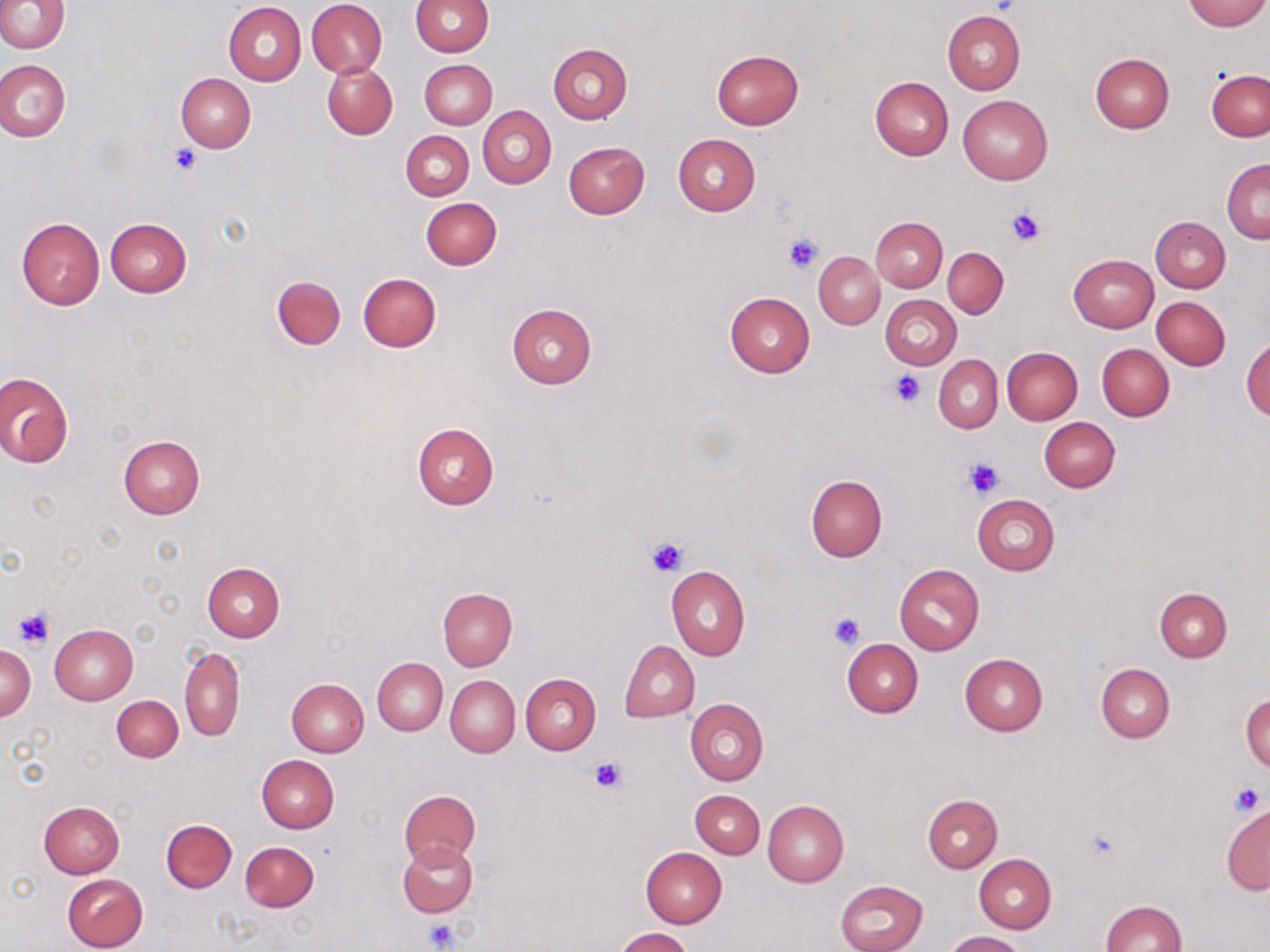 Approximate bounding boxes as named x1/y1/x2/y2 corners in pixels. Platelet locations: (x1=987, y1=0, x2=1021, y2=16), (x1=171, y1=145, x2=200, y2=174), (x1=1005, y1=206, x2=1047, y2=250), (x1=783, y1=232, x2=822, y2=273), (x1=887, y1=371, x2=924, y2=408), (x1=962, y1=457, x2=1007, y2=500), (x1=644, y1=536, x2=688, y2=577), (x1=13, y1=608, x2=55, y2=647), (x1=829, y1=612, x2=864, y2=649), (x1=590, y1=756, x2=625, y2=792), (x1=1230, y1=782, x2=1266, y2=814), (x1=424, y1=918, x2=458, y2=952). Uninfected red blood cell locations: (x1=0, y1=0, x2=68, y2=53), (x1=307, y1=0, x2=387, y2=78), (x1=413, y1=0, x2=493, y2=56), (x1=1183, y1=0, x2=1269, y2=30), (x1=223, y1=3, x2=306, y2=85), (x1=941, y1=12, x2=1024, y2=94), (x1=548, y1=44, x2=632, y2=124), (x1=711, y1=50, x2=803, y2=130), (x1=1089, y1=52, x2=1173, y2=132), (x1=0, y1=58, x2=70, y2=142), (x1=420, y1=59, x2=496, y2=128), (x1=322, y1=61, x2=398, y2=140), (x1=1206, y1=70, x2=1269, y2=141), (x1=176, y1=74, x2=255, y2=152), (x1=869, y1=76, x2=953, y2=160), (x1=958, y1=95, x2=1052, y2=185), (x1=478, y1=106, x2=556, y2=189), (x1=401, y1=130, x2=474, y2=201), (x1=673, y1=133, x2=760, y2=215), (x1=564, y1=142, x2=650, y2=218), (x1=1221, y1=159, x2=1270, y2=244), (x1=421, y1=198, x2=502, y2=269), (x1=1151, y1=216, x2=1231, y2=291), (x1=871, y1=217, x2=947, y2=292), (x1=16, y1=218, x2=105, y2=310), (x1=104, y1=218, x2=191, y2=298), (x1=942, y1=247, x2=1008, y2=318), (x1=814, y1=251, x2=884, y2=329), (x1=1069, y1=253, x2=1158, y2=332), (x1=358, y1=273, x2=442, y2=352), (x1=272, y1=276, x2=346, y2=349), (x1=724, y1=292, x2=814, y2=378), (x1=880, y1=295, x2=961, y2=369), (x1=1151, y1=295, x2=1231, y2=370), (x1=506, y1=303, x2=597, y2=388), (x1=1242, y1=338, x2=1270, y2=420), (x1=1097, y1=344, x2=1174, y2=422), (x1=1002, y1=346, x2=1082, y2=425), (x1=934, y1=355, x2=1003, y2=432), (x1=0, y1=372, x2=74, y2=467), (x1=1040, y1=417, x2=1120, y2=492), (x1=412, y1=422, x2=499, y2=509), (x1=118, y1=435, x2=204, y2=519), (x1=805, y1=474, x2=887, y2=562), (x1=972, y1=494, x2=1061, y2=576), (x1=202, y1=562, x2=284, y2=641), (x1=894, y1=563, x2=985, y2=655), (x1=666, y1=565, x2=750, y2=661), (x1=1154, y1=587, x2=1232, y2=662), (x1=438, y1=589, x2=517, y2=670), (x1=48, y1=624, x2=137, y2=704), (x1=843, y1=639, x2=923, y2=718), (x1=620, y1=640, x2=700, y2=722), (x1=0, y1=643, x2=36, y2=720), (x1=179, y1=646, x2=245, y2=743), (x1=959, y1=653, x2=1047, y2=735), (x1=372, y1=657, x2=446, y2=734), (x1=1096, y1=663, x2=1174, y2=744), (x1=520, y1=672, x2=601, y2=754), (x1=446, y1=676, x2=519, y2=757), (x1=286, y1=678, x2=369, y2=756), (x1=112, y1=694, x2=183, y2=762), (x1=1242, y1=696, x2=1270, y2=773), (x1=685, y1=698, x2=768, y2=785), (x1=257, y1=754, x2=339, y2=832), (x1=399, y1=789, x2=480, y2=865), (x1=689, y1=790, x2=764, y2=857), (x1=923, y1=794, x2=1002, y2=872), (x1=763, y1=800, x2=849, y2=886), (x1=39, y1=801, x2=124, y2=877), (x1=1220, y1=805, x2=1269, y2=896), (x1=161, y1=819, x2=236, y2=892), (x1=240, y1=841, x2=319, y2=912), (x1=398, y1=842, x2=477, y2=917), (x1=641, y1=847, x2=727, y2=927), (x1=974, y1=854, x2=1056, y2=933), (x1=61, y1=873, x2=149, y2=952), (x1=835, y1=879, x2=928, y2=952), (x1=1099, y1=900, x2=1186, y2=952), (x1=615, y1=927, x2=694, y2=952), (x1=945, y1=931, x2=1028, y2=951). Slide-level diagnosis: no evidence of blood parasites. Light microscopy. Single field of view. Image is 1270×952 pixels. Captured at 1000x magnification. Thin blood film. May-Grünwald-Giemsa stain.